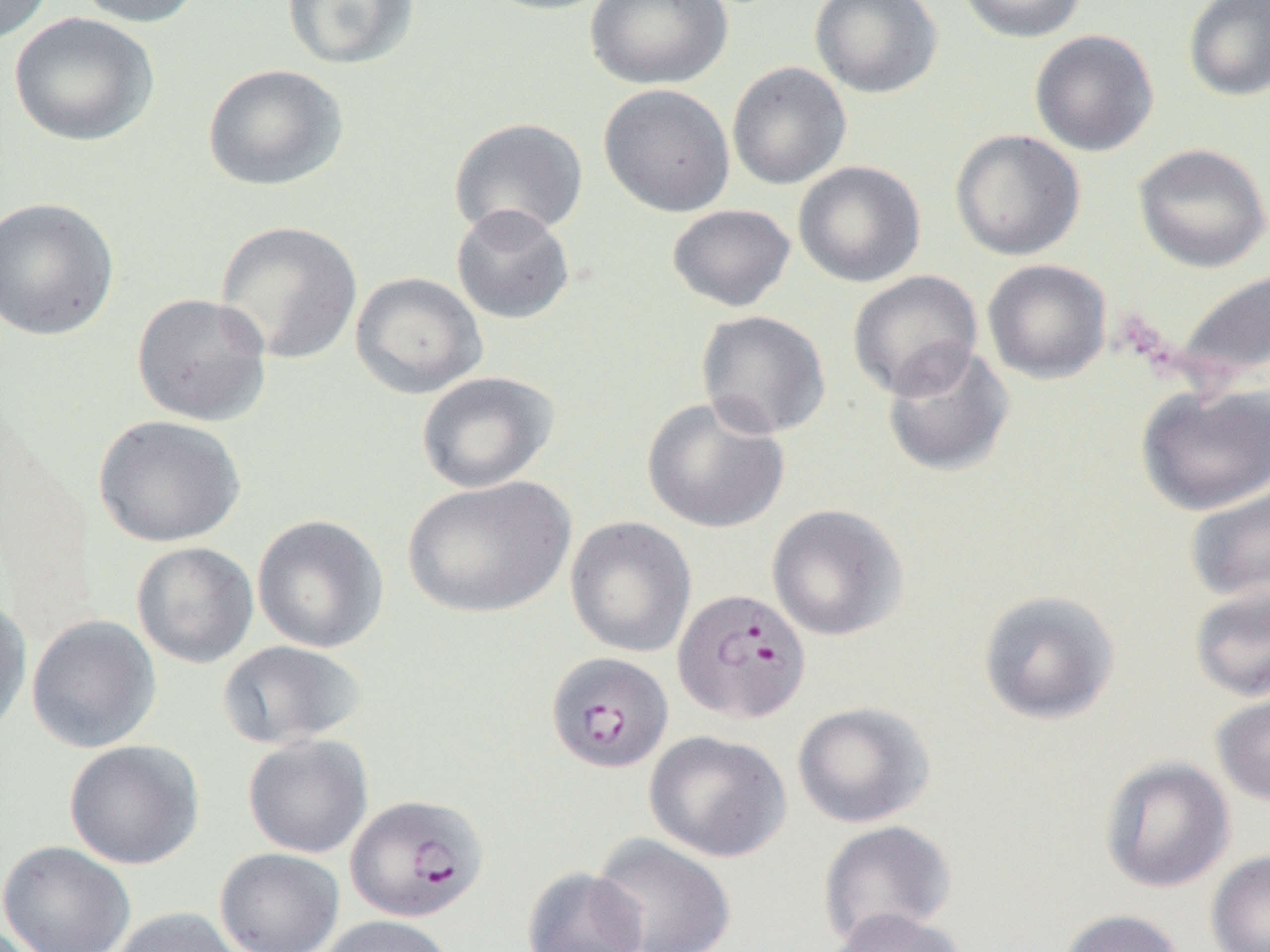
Approximate bounding boxes as (x1,y1)-(x2,y2) corner pairs in pixels. Plasmodium falciparum-infected red blood cell locations: (672,588)-(811,723), (545,652)-(673,773), (345,793)-(489,923). Uninfected red blood cell locations: (0,0)-(54,45), (73,0)-(204,28), (282,0)-(420,70), (475,0)-(618,16), (585,0)-(732,91), (809,0)-(943,99), (956,0)-(1088,44), (1182,0)-(1270,101), (9,12)-(159,147), (1029,30)-(1159,156), (726,62)-(852,190), (202,63)-(348,191), (598,83)-(735,217), (449,117)-(589,239), (950,129)-(1086,261), (1132,143)-(1270,273), (792,160)-(926,288), (0,196)-(120,341), (667,203)-(797,312), (450,204)-(575,325), (215,220)-(363,365), (982,259)-(1112,384), (1172,267)-(1270,385), (847,270)-(983,401), (350,272)-(487,399), (131,292)-(273,427), (695,310)-(831,440), (881,341)-(1015,479), (416,371)-(558,493), (1135,383)-(1270,516), (641,396)-(790,534), (93,414)-(245,548), (401,475)-(575,619), (1184,479)-(1270,605), (766,504)-(909,642), (251,514)-(389,653), (565,516)-(697,658), (131,542)-(259,668), (1189,583)-(1270,702), (977,588)-(1121,726), (0,595)-(33,739), (26,615)-(162,754), (217,640)-(366,750), (1211,688)-(1270,807), (792,701)-(934,828), (645,730)-(791,862), (243,734)-(373,857), (64,739)-(205,870), (1099,755)-(1235,893), (817,819)-(957,948), (590,832)-(736,952), (0,840)-(137,952), (214,847)-(345,952), (1206,850)-(1270,952), (521,866)-(649,952), (110,906)-(248,952), (825,907)-(968,952), (1058,908)-(1185,952), (315,915)-(457,952). Slide-level diagnosis: Plasmodium falciparum. Image is 1270×952 pixels. Thin blood smear. Single field of view. Optical microscopy. 1000x magnification.